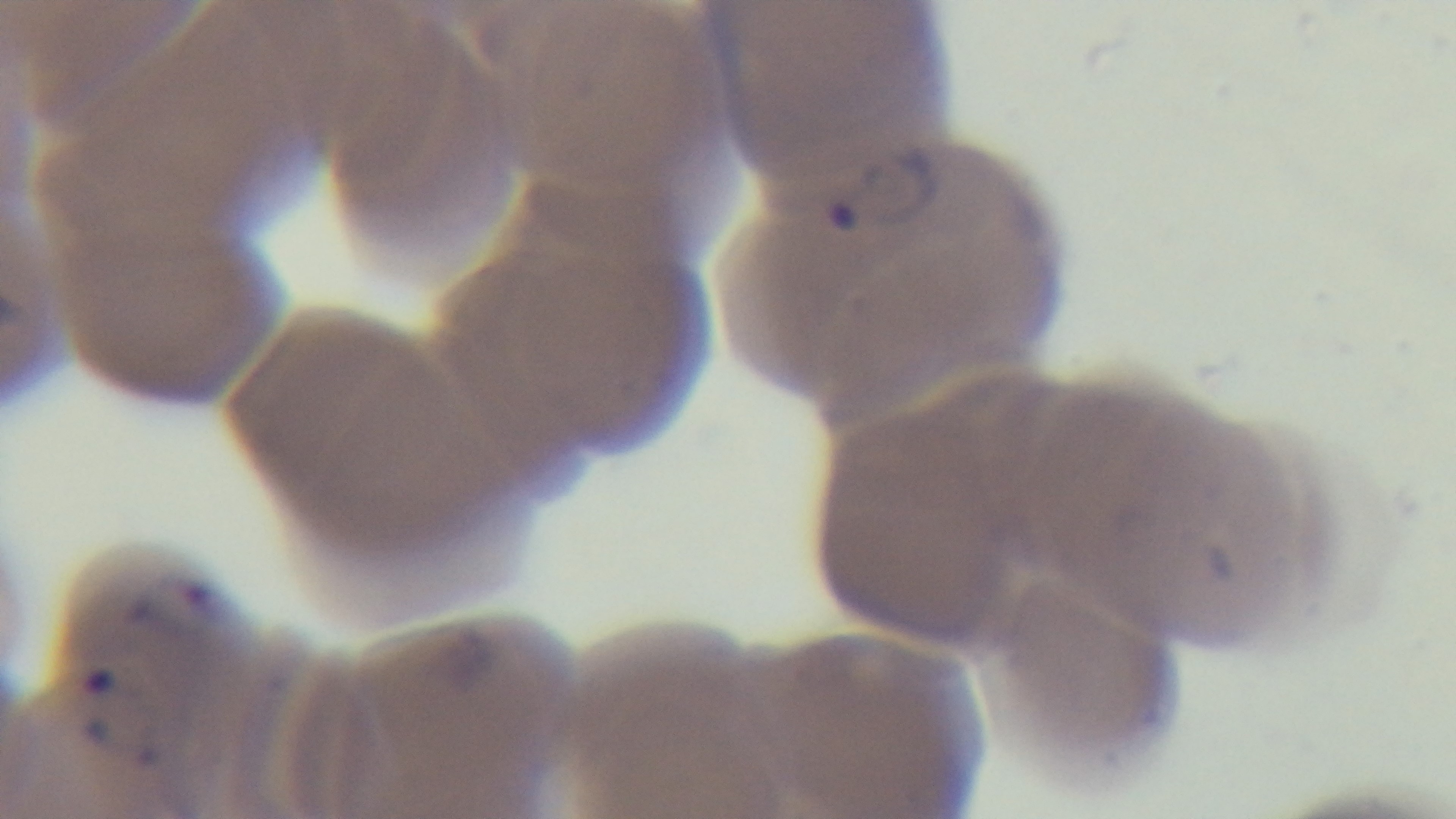
Malaria status: infected. 100x oil-immersion objective. Light microscopy. One field from the slide. Mounted 4K digital camera. Giemsa stain. Preparation: thin.